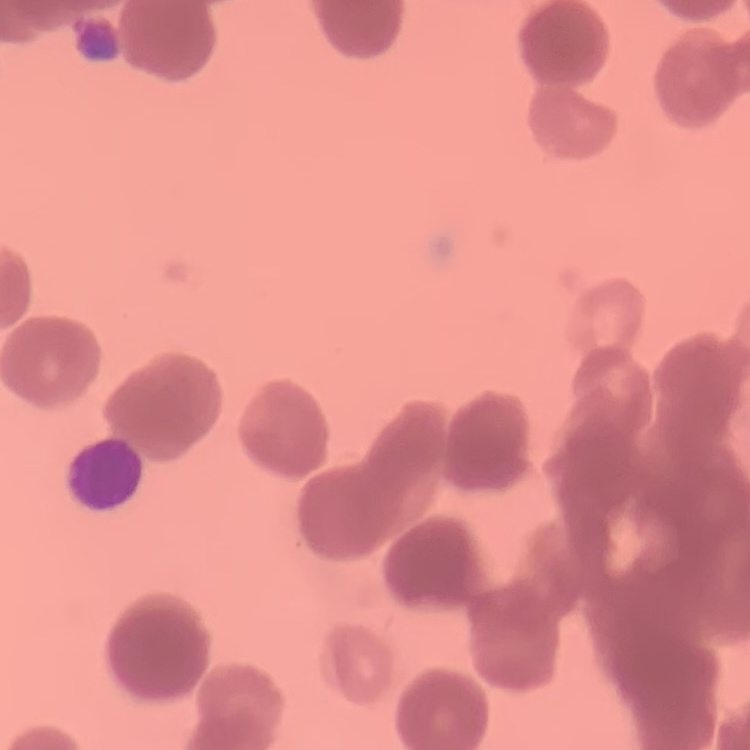

Summary:
  - Erythrocyte morphology: rouleaux formation
  - Preparation: thin peripheral smear
  - Image type: one tile cut from a larger photomicrograph
  - Stain: Field's or Giemsa